Give the position of every Plasmodium parasite visible.
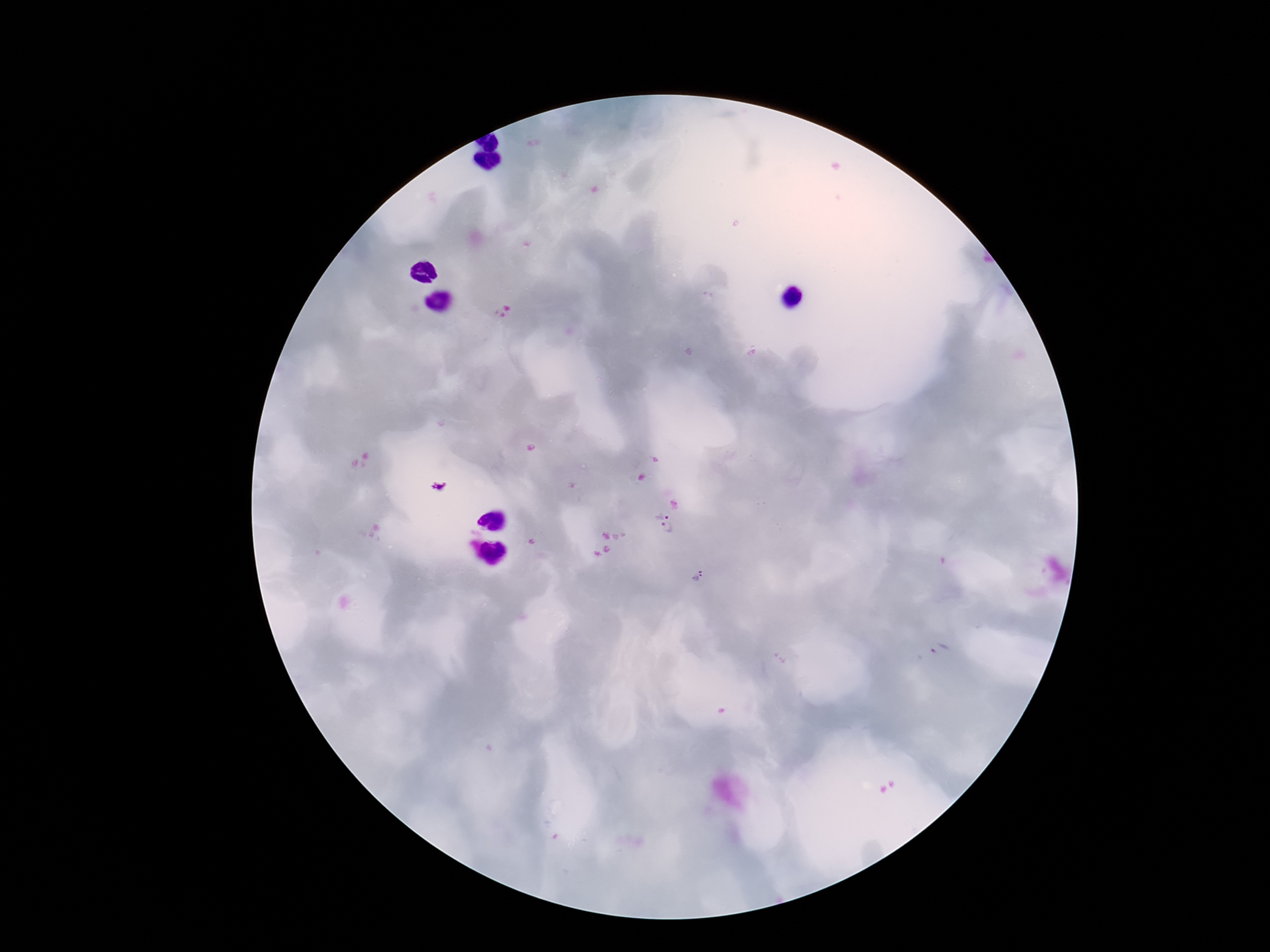
Approximate centers as (x, y) in pixels.
Plasmodium parasites: (662, 513), (670, 531), (698, 578), (939, 650).

Patient malaria status: positive. Single field of view. Photographed through the microscope eyepiece with a smartphone camera. Thick blood film. Giemsa stain. Image is 1270×952 pixels. 100x magnification.